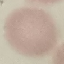

malaria status = uninfected
capture = smartphone through the microscope eyepiece
preparation = thin blood smear
image type = automatically extracted cell patch, resized to 64 × 64 pixels
stain = Giemsa